Identify the cell.
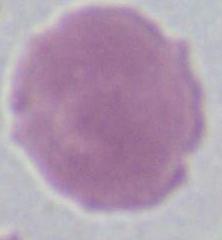

An erythrocyte.

Captured at 1000x magnification. Photomicrograph.